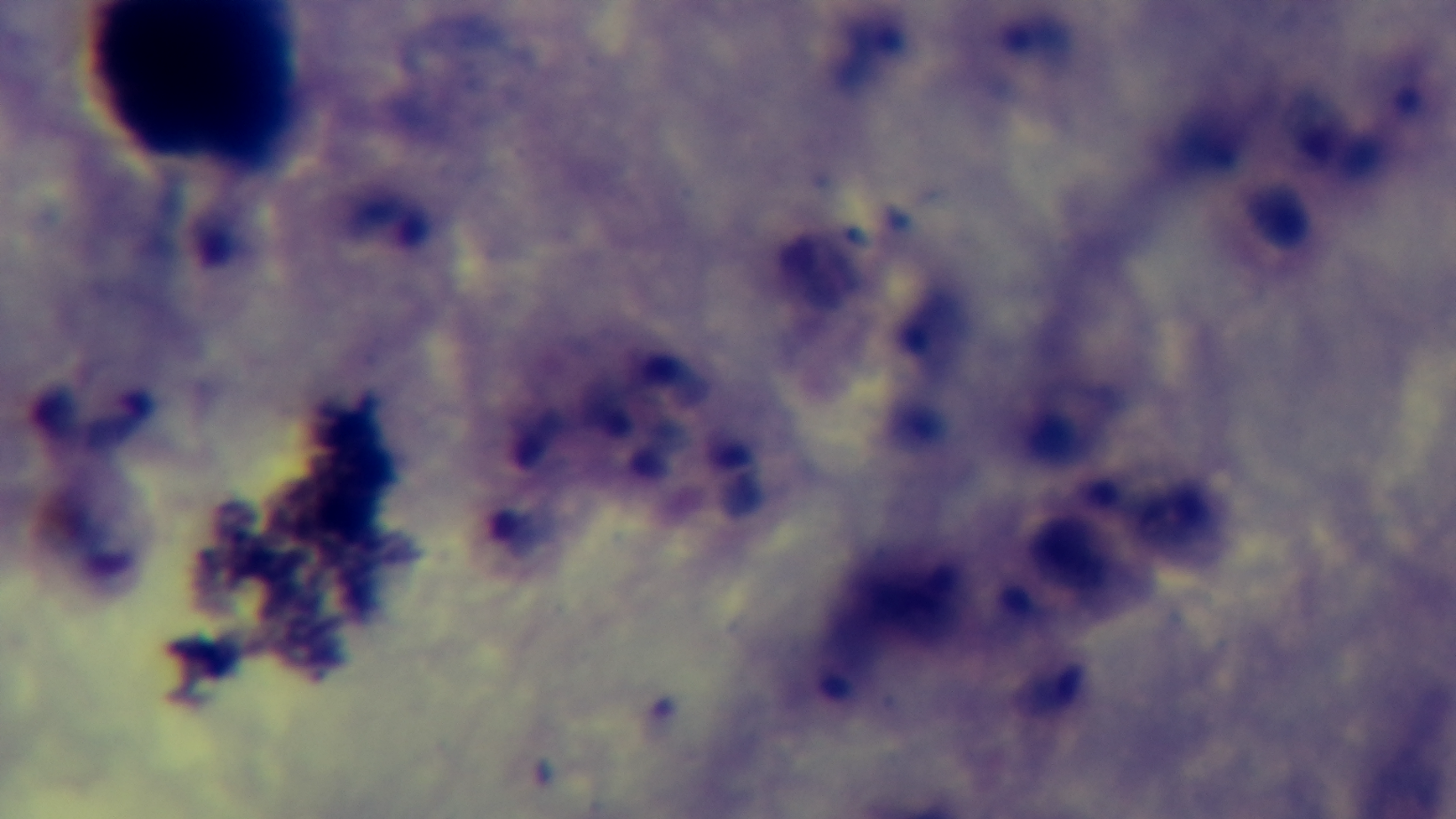
Malaria status: positive. Giemsa-stained. Single field of view. Photomicrograph. Oil-immersion objective, 100x. Preparation: thick blood film. Mounted 4K digital camera.